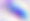
Captured at 400x magnification. Photomicrograph. Toxoplasma gondii is seen.